Locate and identify every blood parasite.
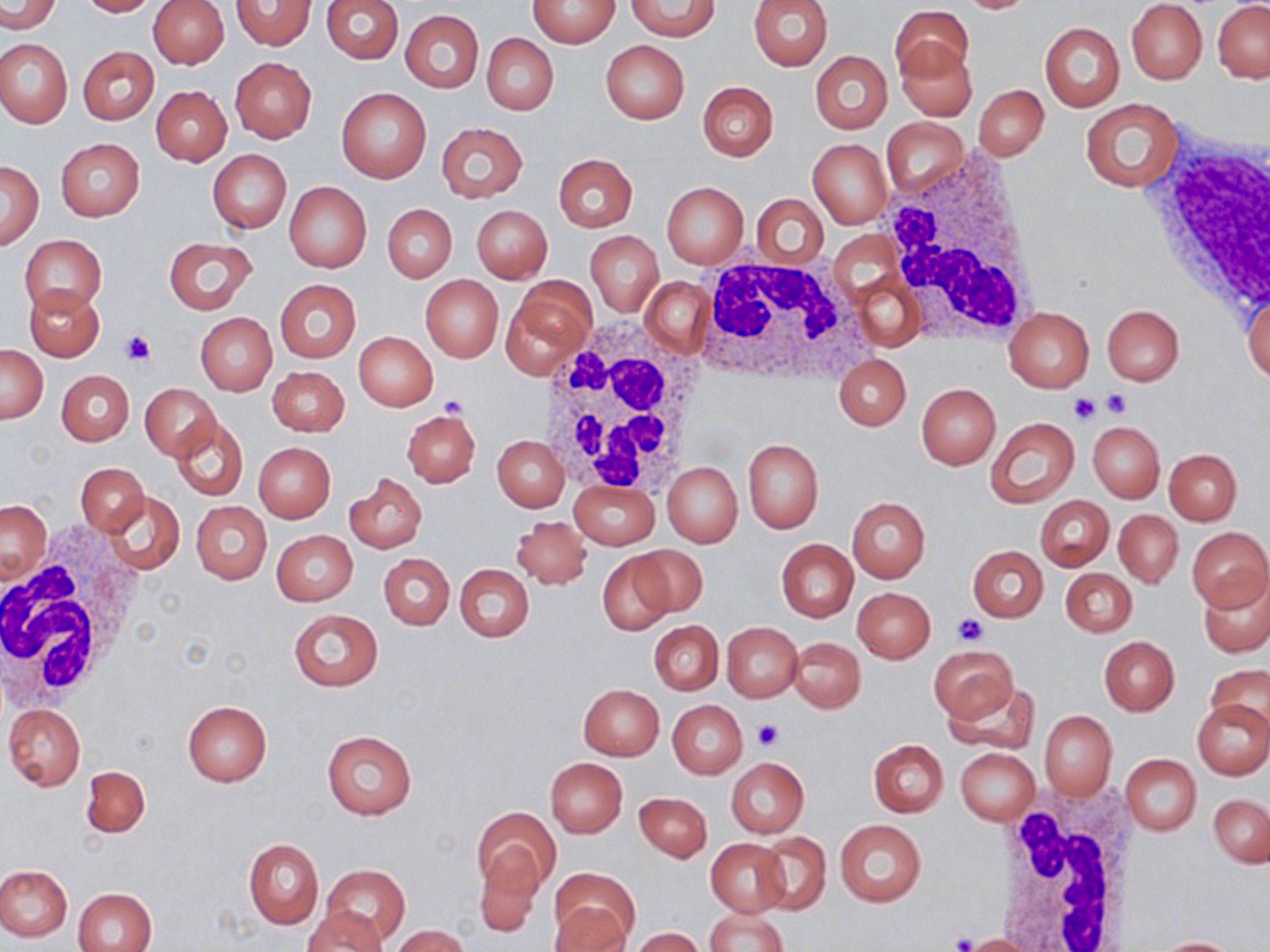
No blood parasites seen.

Summary:
  - Coordinate format: approximate bounding boxes as (x1, y1, x2, y2) in pixels
  - White blood cell locations: (1141, 132, 1269, 322), (879, 150, 1043, 345), (692, 256, 867, 382), (536, 320, 710, 494), (0, 523, 146, 714), (986, 785, 1144, 952)
  - Uninfected red blood cell locations: (76, 0, 160, 16), (322, 0, 403, 63), (747, 0, 832, 70), (955, 0, 1039, 13), (1, 1, 59, 34), (148, 1, 228, 69), (230, 1, 316, 49), (529, 1, 621, 48), (627, 1, 719, 41), (1125, 1, 1208, 85), (1212, 1, 1270, 82), (891, 4, 972, 81), (400, 11, 483, 92), (1040, 22, 1124, 112), (481, 33, 559, 115), (0, 39, 72, 128), (601, 40, 690, 123), (895, 42, 978, 121), (78, 46, 158, 124), (811, 50, 892, 133), (230, 57, 316, 142), (697, 82, 777, 160), (974, 85, 1049, 160), (152, 86, 231, 165), (336, 87, 431, 183), (1081, 100, 1184, 192), (883, 121, 967, 198), (435, 123, 527, 202), (56, 139, 144, 221), (809, 139, 892, 228), (208, 149, 291, 233), (553, 154, 637, 231), (0, 161, 43, 249), (284, 182, 372, 272), (662, 182, 748, 268), (752, 195, 827, 270), (382, 205, 456, 281), (471, 205, 551, 283), (586, 231, 663, 317), (20, 235, 107, 314), (164, 236, 256, 313), (849, 272, 924, 351), (421, 276, 503, 360), (640, 277, 713, 357), (274, 279, 360, 363), (24, 285, 104, 360), (502, 286, 592, 378), (1244, 290, 1270, 386), (1101, 304, 1185, 386), (1003, 306, 1092, 390), (195, 313, 277, 395), (353, 331, 437, 411), (0, 345, 47, 423), (834, 354, 910, 431), (267, 366, 349, 436), (56, 369, 135, 446), (139, 383, 221, 459), (916, 383, 1000, 469), (403, 410, 480, 487), (171, 416, 248, 500), (986, 417, 1079, 507), (1087, 420, 1163, 502), (493, 435, 569, 511), (743, 438, 824, 534), (253, 442, 336, 522), (1164, 449, 1242, 524), (668, 451, 818, 536), (662, 461, 742, 547), (77, 463, 148, 535), (345, 473, 426, 553), (569, 481, 660, 549), (103, 491, 184, 576), (1036, 496, 1113, 570), (847, 498, 930, 582), (1, 500, 51, 582), (191, 501, 271, 583), (1114, 509, 1183, 588), (511, 516, 592, 589), (1186, 526, 1270, 612), (271, 530, 357, 606), (777, 539, 858, 622), (630, 545, 708, 618), (968, 546, 1048, 622), (380, 553, 454, 630), (597, 553, 676, 635), (455, 564, 534, 641), (1061, 567, 1136, 636), (1197, 570, 1270, 658), (852, 587, 934, 662), (289, 609, 383, 691), (649, 621, 723, 694), (720, 622, 803, 702), (1099, 636, 1179, 714), (787, 637, 865, 713), (928, 644, 1018, 725), (1205, 664, 1270, 732), (943, 680, 1040, 755), (579, 684, 663, 760), (182, 699, 271, 786), (1193, 699, 1269, 780), (667, 700, 747, 778), (4, 704, 86, 790), (1039, 710, 1116, 801), (322, 728, 417, 819), (869, 739, 948, 817), (954, 748, 1039, 825), (1120, 754, 1201, 834), (726, 757, 808, 838), (545, 758, 627, 836), (80, 765, 149, 838), (634, 791, 711, 862), (1209, 793, 1270, 868), (473, 807, 559, 896), (834, 819, 926, 907), (757, 832, 830, 915), (243, 839, 323, 928), (707, 839, 790, 916), (474, 850, 545, 936), (0, 864, 73, 940), (320, 865, 409, 944), (551, 867, 640, 948), (73, 887, 155, 952), (303, 908, 387, 952), (705, 908, 788, 952), (392, 925, 470, 952), (631, 928, 705, 952), (961, 934, 1041, 951), (1151, 936, 1244, 951)
  - Platelet locations: (121, 330, 154, 366), (1101, 390, 1130, 418), (1068, 392, 1099, 425), (440, 395, 469, 417), (952, 614, 988, 646), (752, 719, 784, 750), (952, 932, 977, 951)
  - Slide-level diagnosis: negative for blood parasites
  - Image size: 1270×952 pixels
  - Stain: May-Grünwald-Giemsa
  - Field of view: single
  - Preparation: thin blood film
  - Magnification: 1000x
  - Modality: light microscopy